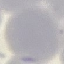
Summary:
  - Result: no malaria parasites detected
  - Preparation: thin blood smear
  - Image type: automatically extracted cell patch, resized to 64 × 64 pixels
  - Capture: smartphone camera at the microscope eyepiece
  - Stain: Giemsa